Classify this cell by malaria status.
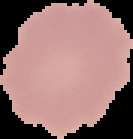
It is uninfected.

Summary:
  - Image type: segmented cell region with the area outside set to black
  - Image size: 133×139 pixels
  - Preparation: thin blood film